Classify this cell by malaria status.
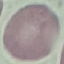

It is uninfected.

stain: Giemsa
capture: smartphone through the microscope eyepiece
image_type: automatically extracted cell patch, resized to 64 × 64 pixels
preparation: thin smear